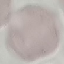
Summary:
  - Result: no malaria parasites detected
  - Preparation: thin smear
  - Stain: Giemsa
  - Image type: cell patch, automatically extracted from a larger field of view and resized to 64 × 64 pixels
  - Capture: smartphone through the microscope eyepiece